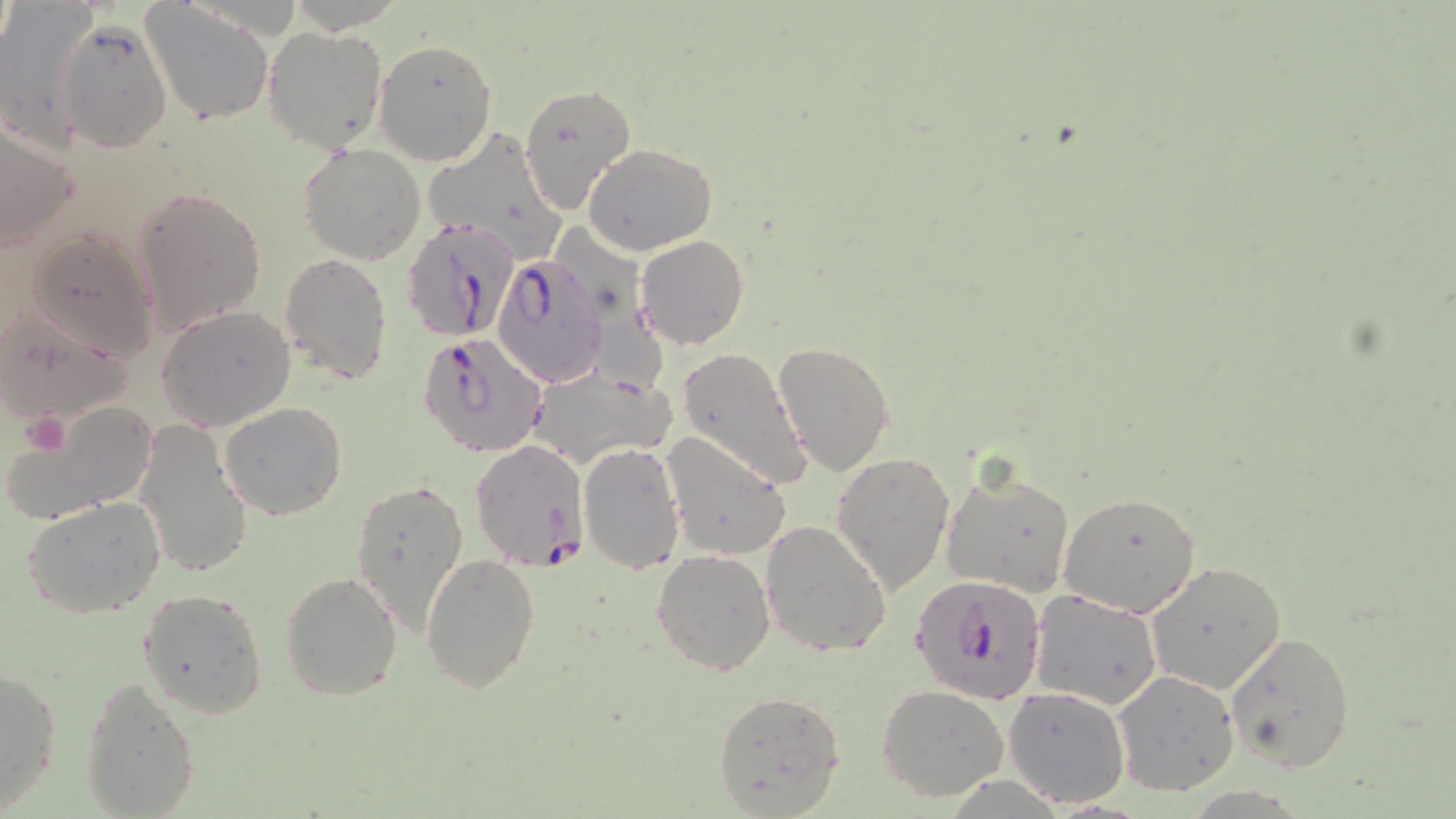

Approximate bounding boxes as (x1,y1)-(x2,y2) corner pairs in pixels. Plasmodium falciparum-infected red blood cell locations: (402,218)-(521,338), (492,255)-(610,388), (417,334)-(547,458), (468,439)-(589,569), (910,573)-(1046,706). Uninfected red blood cell locations: (0,2)-(96,158), (142,2)-(275,127), (56,19)-(172,152), (262,26)-(387,155), (373,38)-(499,167), (517,82)-(636,216), (0,119)-(80,254), (423,127)-(564,265), (297,143)-(426,266), (583,143)-(717,256), (132,186)-(267,334), (23,228)-(159,365), (635,236)-(749,351), (278,251)-(394,384), (1,301)-(135,427), (156,306)-(297,430), (771,340)-(895,475), (678,347)-(815,489), (523,367)-(673,471), (5,399)-(161,524), (218,400)-(348,519), (134,419)-(254,580), (662,432)-(792,563), (578,441)-(684,574), (831,451)-(956,595), (942,468)-(1077,598), (350,478)-(470,632), (1059,491)-(1202,617), (22,495)-(167,619), (759,519)-(892,657), (653,550)-(776,676), (420,552)-(541,693), (1145,561)-(1288,696), (279,570)-(403,702), (138,588)-(269,719), (1031,592)-(1162,710), (1226,630)-(1357,772), (0,665)-(63,810), (1112,670)-(1240,795), (79,675)-(202,819), (877,684)-(1009,802), (1002,686)-(1133,808), (712,690)-(846,817). Platelet locations: (24,411)-(70,456). Slide-level diagnosis: Plasmodium falciparum. Thin blood film. Light microscopy. May-Grünwald-Giemsa stain. 1000x magnification. Single field of view. Image is 1456×819 pixels.